Give the preparation type.
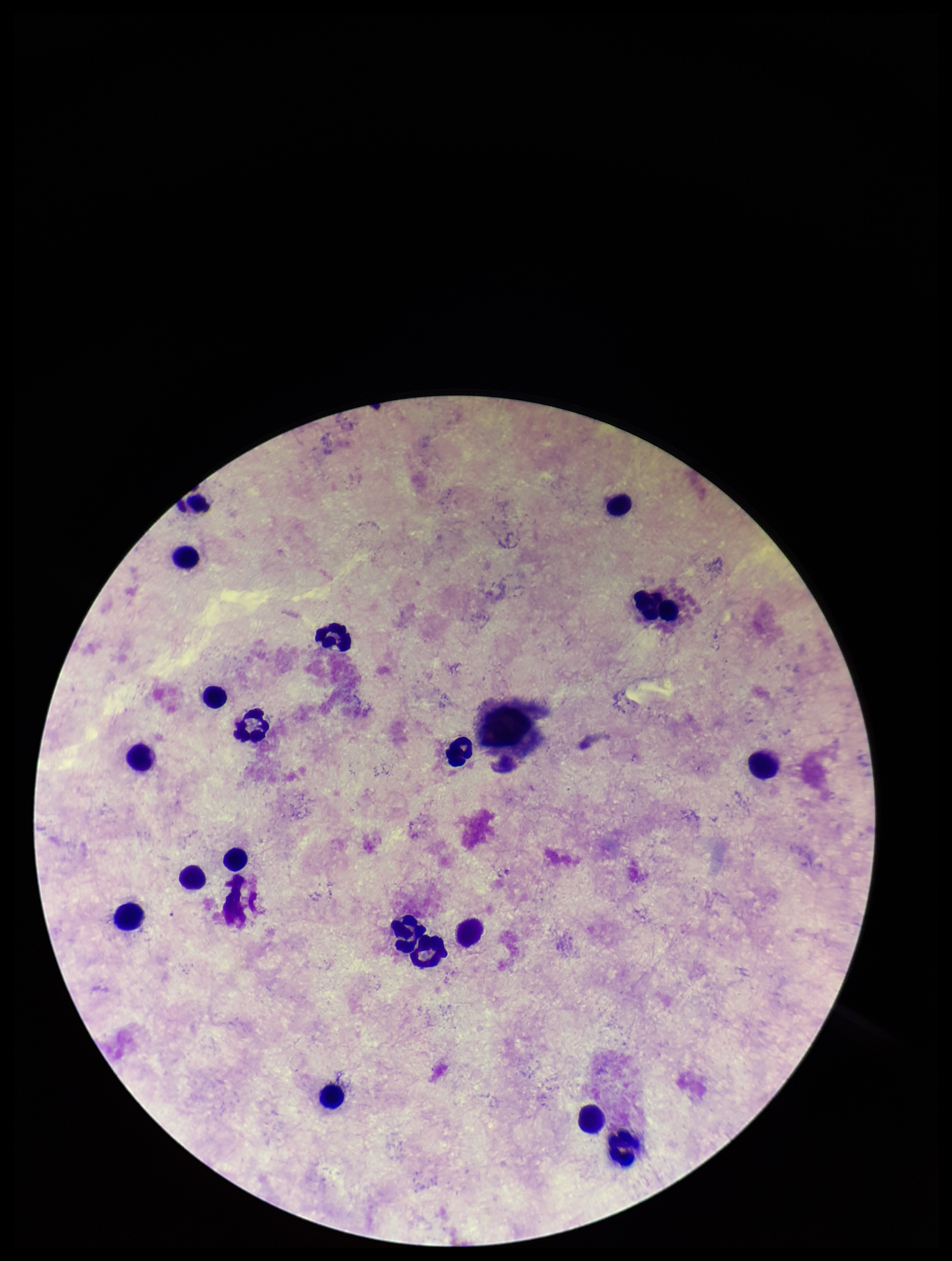

It is a thick blood smear.

image size = 952×1261 pixels
parasite count = 0
leukocyte count = 19
stain = Giemsa
patient malaria status = negative
capture = smartphone photograph through the microscope eyepiece
field of view = one from this slide
Plasmodium parasites = none detected